Locate every leukocyte (white blood cell).
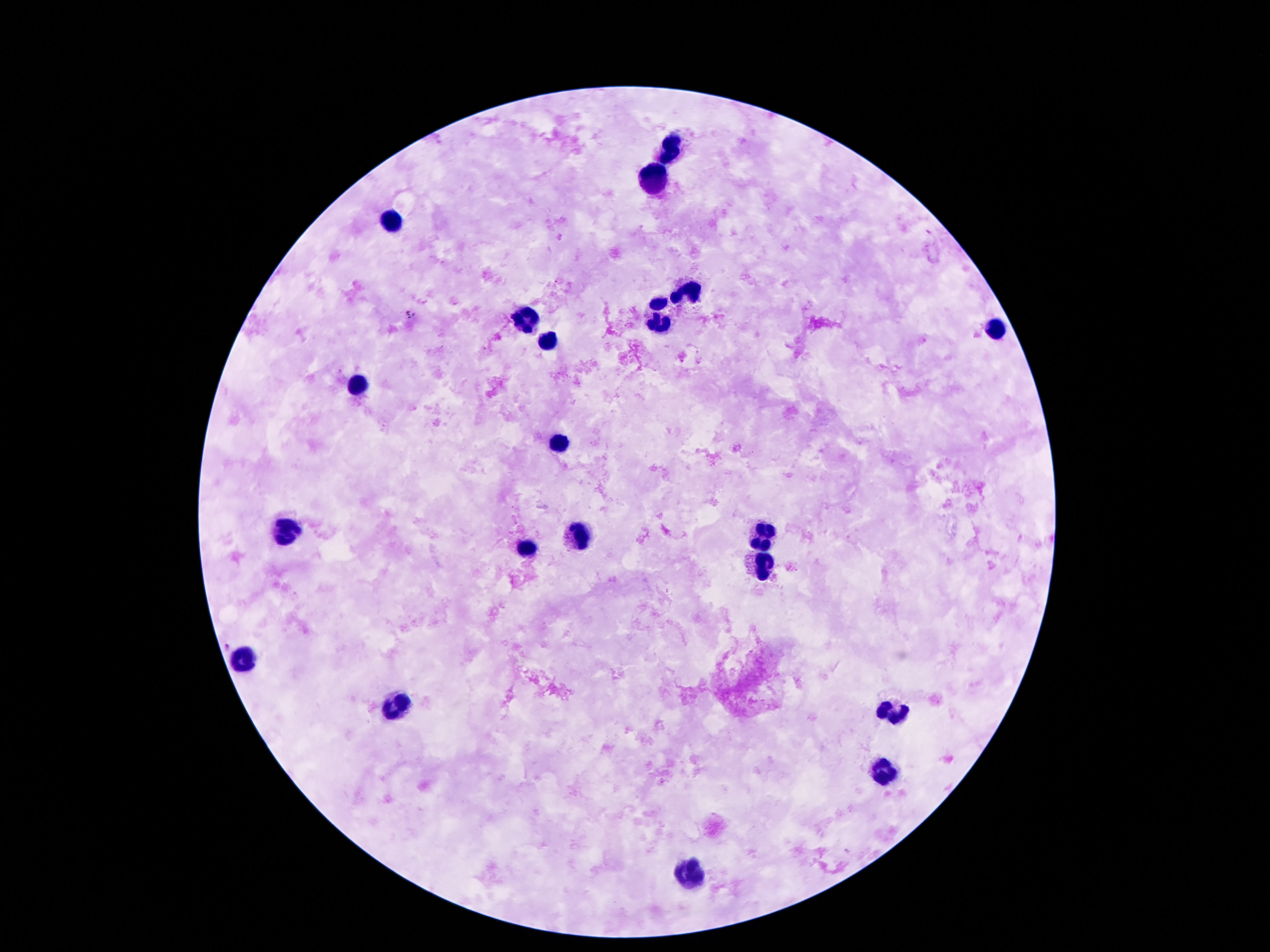

Approximate object centers, in pixels from the top-left corner.
Leukocytes: (x=671, y=150), (x=652, y=176), (x=390, y=219), (x=688, y=293), (x=658, y=301), (x=524, y=318), (x=661, y=324), (x=994, y=331), (x=551, y=341), (x=354, y=387), (x=560, y=444), (x=287, y=533), (x=581, y=533), (x=763, y=535), (x=530, y=548), (x=763, y=563), (x=243, y=657), (x=396, y=705), (x=889, y=714), (x=885, y=770), (x=694, y=874).

capture = smartphone camera through the microscope eyepiece
stain = Giemsa
magnification = 100x
preparation = thick blood smear
field of view = one from this slide
image size = 1270×952 pixels
patient malaria status = negative